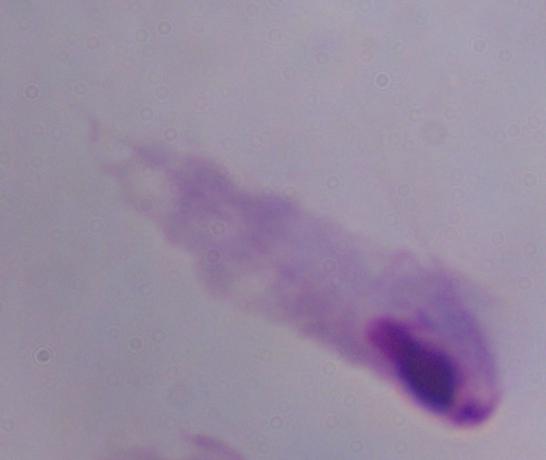

magnification = 1000x
modality = photomicrograph
identification = trichomonad